Report the malaria status of this cell.
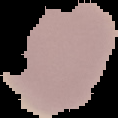

It is uninfected.

{
  "image_type": "segmented cell region with the area outside set to black",
  "image_size": "118×118 pixels",
  "preparation": "thin blood smear"
}